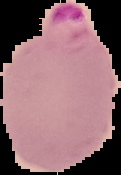
Summary:
  - Result: malaria parasites detected
  - Preparation: thin blood smear
  - Image size: 121×175 pixels
  - Image type: cell region segmented out of the field of view; surrounding area masked to black